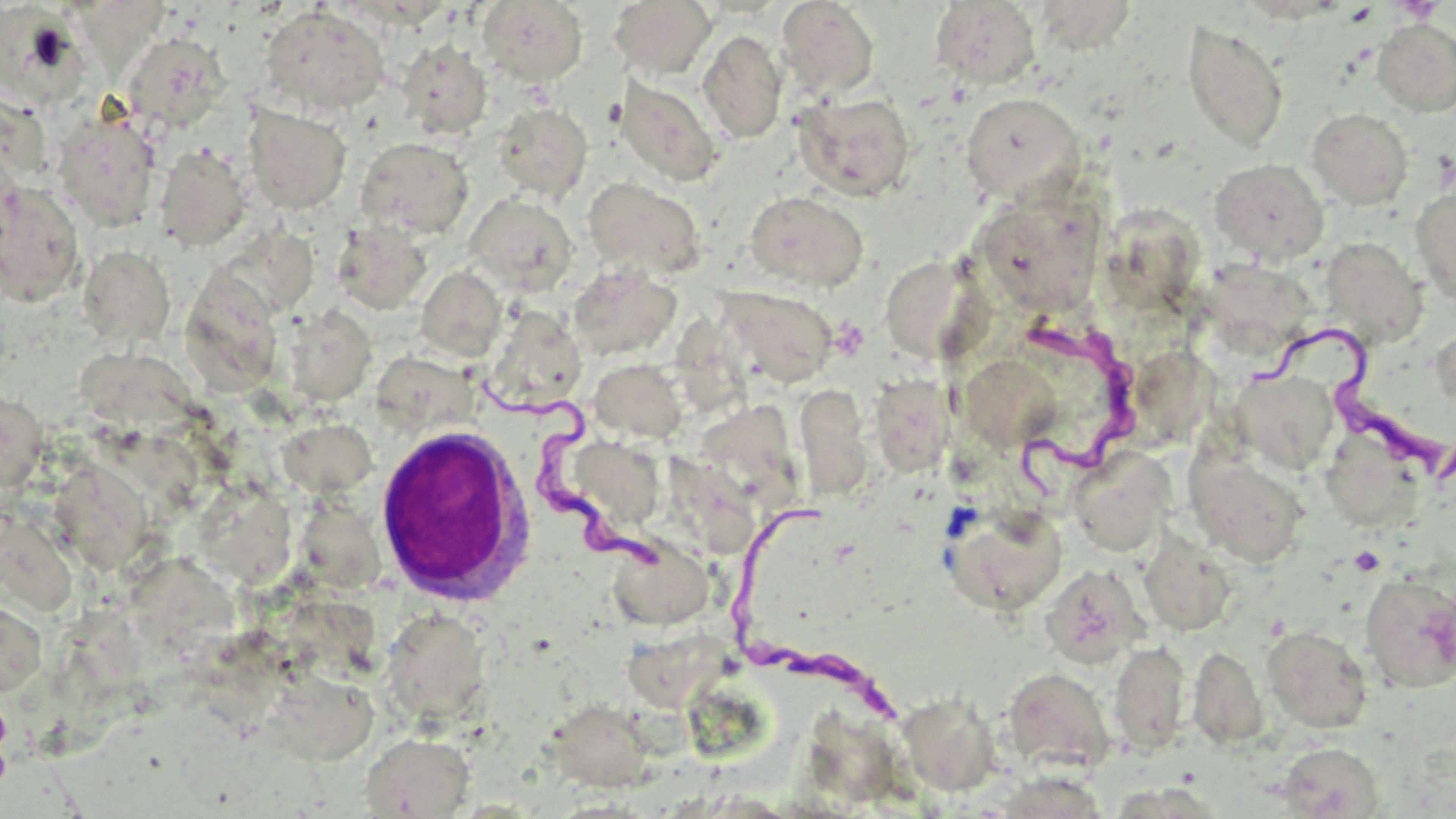

Summary:
  - Coordinate format: approximate bounding boxes as [x1, y1, x2, y2] in pixels
  - White blood cell locations: [373, 424, 534, 605]
  - Trypanosoma brucei locations: [1008, 317, 1140, 501], [1260, 328, 1444, 485], [479, 373, 668, 582], [727, 499, 905, 723]
  - Platelet locations: [1344, 4, 1378, 25], [1348, 545, 1386, 576]
  - Uninfected red blood cell locations: [476, 0, 588, 86], [609, 0, 717, 79], [776, 1, 880, 100], [930, 1, 1041, 89], [1039, 2, 1134, 60], [259, 5, 391, 116], [1, 6, 96, 104], [71, 10, 172, 84], [1372, 18, 1456, 118], [1181, 20, 1288, 152], [698, 29, 787, 144], [122, 32, 228, 132], [398, 39, 493, 139], [615, 75, 724, 186], [795, 92, 915, 201], [960, 92, 1085, 204], [493, 103, 592, 201], [3, 104, 59, 182], [244, 105, 351, 214], [1307, 108, 1413, 210], [53, 110, 161, 231], [356, 136, 474, 239], [155, 144, 252, 251], [1209, 159, 1329, 264], [582, 176, 707, 281], [0, 181, 85, 307], [988, 183, 1114, 309], [1411, 185, 1456, 307], [744, 191, 868, 292], [464, 194, 579, 296], [1111, 210, 1207, 317], [331, 222, 432, 315], [240, 223, 323, 308], [1320, 237, 1428, 347], [78, 246, 175, 347], [885, 259, 993, 367], [1211, 263, 1314, 353], [567, 264, 682, 360], [416, 266, 507, 361], [178, 267, 283, 397], [716, 287, 840, 387], [673, 305, 760, 423], [282, 306, 377, 407], [484, 306, 587, 412], [1431, 325, 1456, 416], [83, 352, 206, 435], [965, 356, 1054, 456], [379, 358, 475, 431], [1149, 358, 1223, 443], [589, 359, 688, 444], [1232, 370, 1337, 473], [870, 376, 956, 476], [796, 383, 873, 501], [0, 388, 48, 495], [706, 407, 804, 511], [281, 420, 378, 498], [99, 430, 209, 515], [557, 436, 668, 536], [1066, 446, 1176, 557], [1187, 453, 1309, 568], [664, 454, 751, 558], [52, 455, 154, 582], [198, 480, 299, 592], [5, 505, 86, 621], [947, 506, 1068, 615], [306, 510, 389, 592], [615, 530, 712, 641], [1139, 533, 1237, 636], [141, 558, 240, 656], [1040, 564, 1150, 668], [1359, 573, 1456, 692], [0, 595, 47, 699], [52, 604, 135, 715], [290, 606, 379, 672], [380, 607, 491, 727], [1262, 625, 1373, 733], [639, 632, 741, 707], [198, 633, 296, 734], [1109, 640, 1190, 755], [1188, 644, 1268, 749], [1002, 668, 1116, 774], [284, 680, 375, 759], [0, 684, 13, 801], [897, 692, 1002, 795], [548, 699, 656, 789], [803, 712, 902, 800], [361, 733, 475, 818], [1276, 742, 1384, 818], [992, 766, 1111, 819]
  - Slide-level diagnosis: Trypanosoma brucei
  - Stain: May-Grünwald-Giemsa
  - Field of view: one of a larger specimen
  - Image size: 1456×819 pixels
  - Preparation: thin blood smear
  - Magnification: 1000x
  - Modality: light microscopy